Identify the parasite.
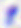

Toxoplasma gondii.

{
  "magnification": "400x",
  "modality": "photomicrograph"
}